Describe the morphology of the erythrocytes.
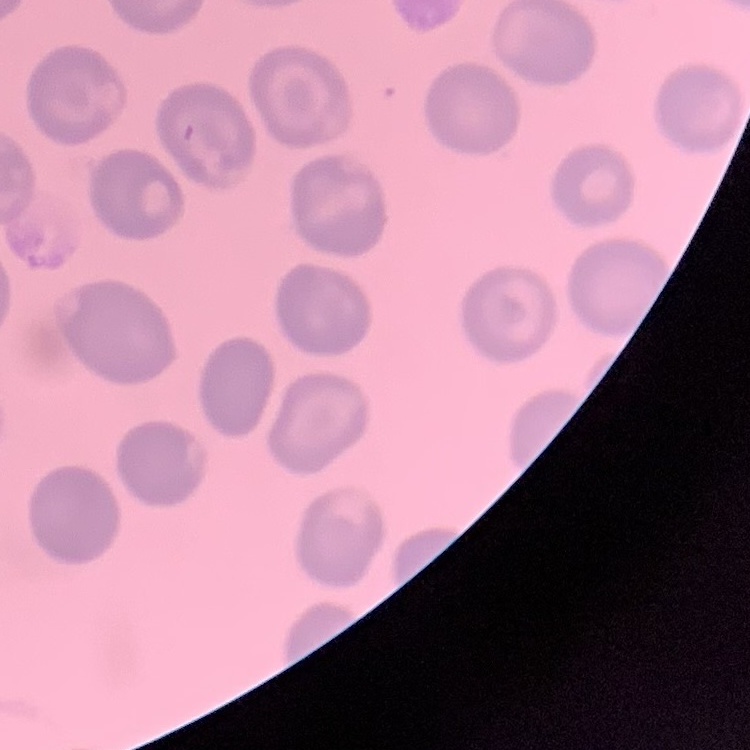
They show no rouleaux formation.

Summary:
  - Image type: one tile cut from a larger photomicrograph
  - Stain: Field's or Giemsa
  - Preparation: thin peripheral smear